Report the malaria status of this cell.
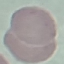
It is uninfected.

Acquired by smartphone through the microscope eyepiece. Thin blood film. Giemsa stain. Automatically extracted cell patch, resized to 64 × 64 pixels.